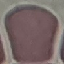
Summary:
  - Malaria status: uninfected
  - Stain: Giemsa
  - Capture: smartphone camera at the microscope eyepiece
  - Preparation: thin blood smear
  - Image type: cell patch, automatically extracted from a larger field of view and resized to 64 × 64 pixels